Identify the parasite.
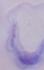
This is a trypanosome.

magnification = 1000x
modality = micrograph